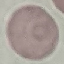

Summary:
  - Malaria status: uninfected
  - Stain: Giemsa
  - Capture: smartphone camera at the microscope eyepiece
  - Preparation: thin blood film
  - Image type: automatically extracted cell patch, resized to 64 × 64 pixels